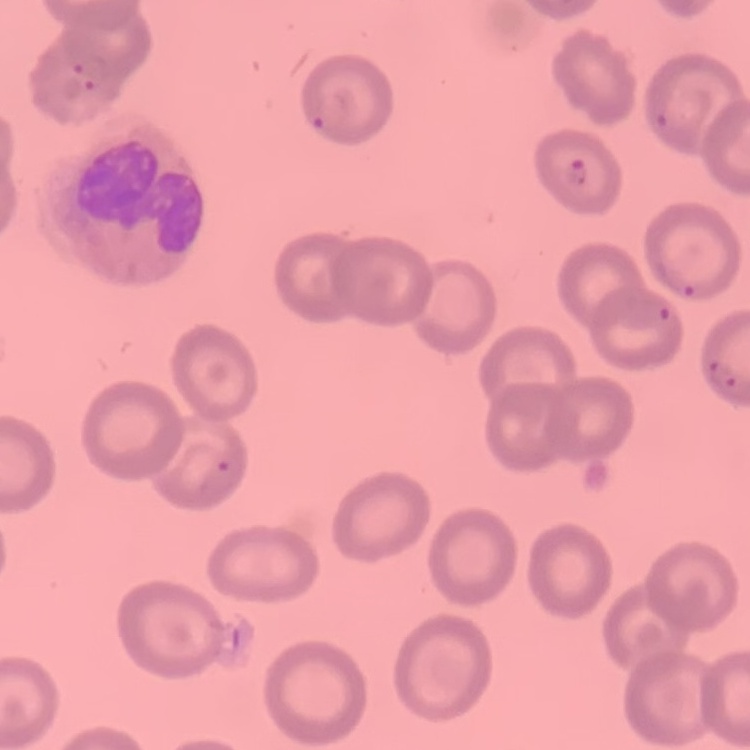 The red blood cells exhibit no rouleaux formation. One tile cut from a larger photomicrograph. Thin blood film. Field's or Giemsa stain.